Assess this cell for malaria.
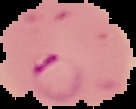
It is parasitized.

Summary:
  - Image type: segmented cell region with the area outside set to black
  - Preparation: thin blood smear
  - Image size: 136×109 pixels